Give the position of every leukocyte.
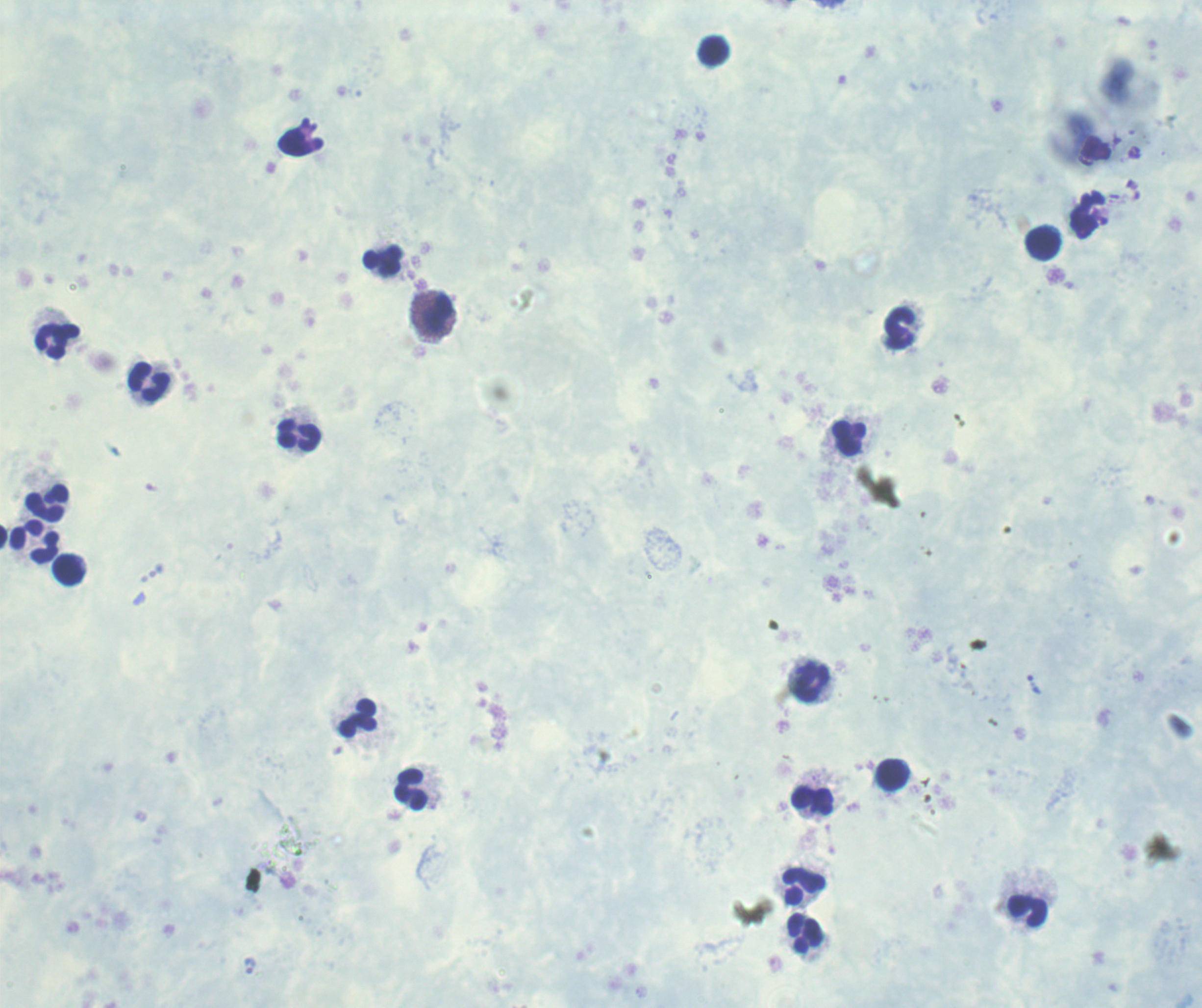

Approximate centers as [x, y] in pixels.
Leukocytes: [715, 51], [1042, 243], [382, 261], [437, 314], [901, 326], [58, 341], [151, 382], [300, 435], [850, 439], [47, 502], [34, 542], [69, 570], [813, 683], [358, 719], [893, 775], [413, 789], [814, 799], [805, 886], [1028, 910], [806, 934].

coordinate format = approximate centers as [x, y] in pixels
trophozoite locations = [1034, 684]
magnification = 100x
image size = 1202×1008 pixels
stain = Romanowsky
preparation = thick blood smear
context = previously used in a real diagnosis
result = malaria parasites detected
field of view = single
background quality = unsatisfactory